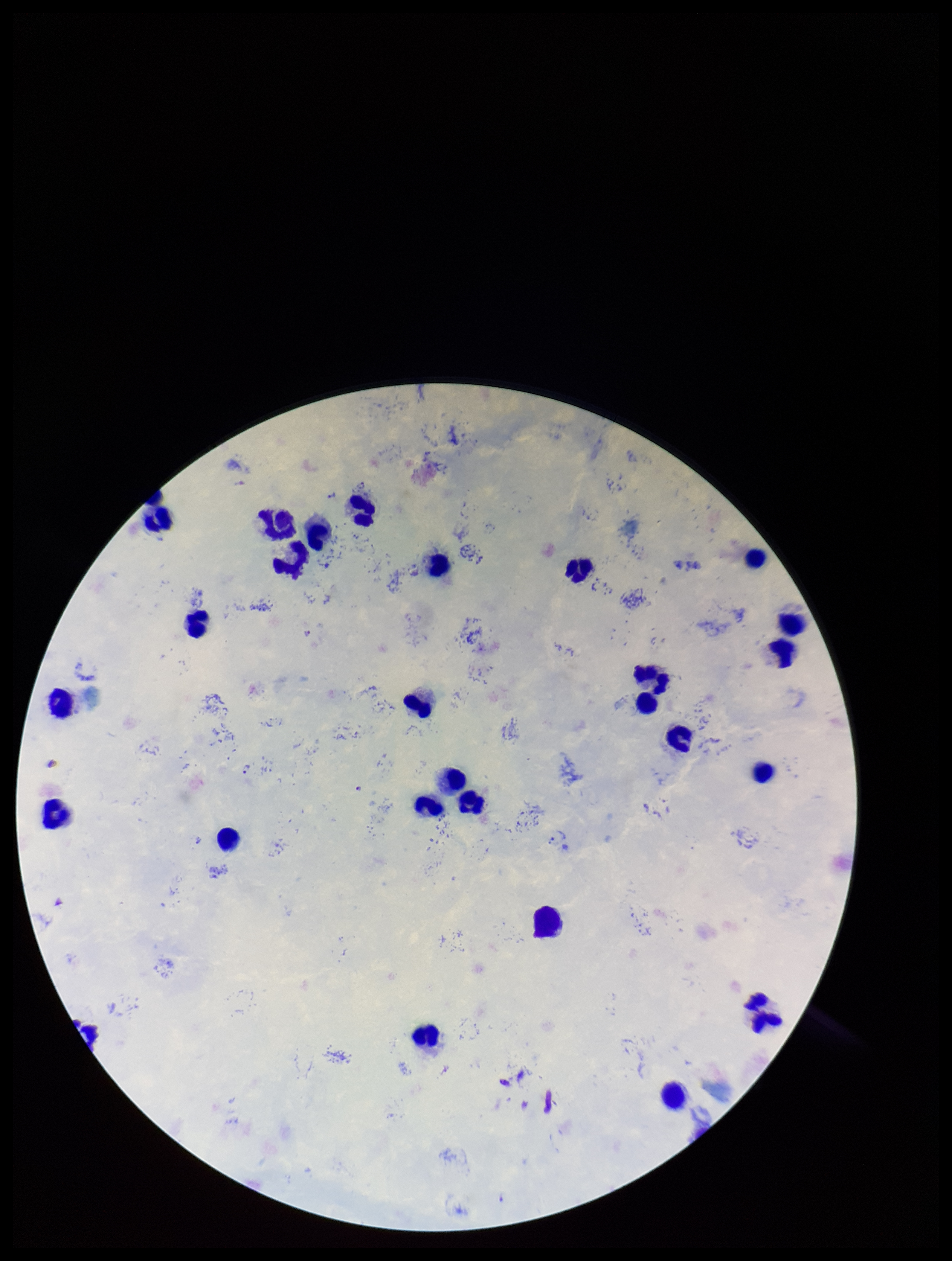
Preparation: thick smear. Plasmodium parasites: seen. Single field of view. Leukocyte count: 25. Smartphone photograph taken through the eyepiece of a microscope. Stained with Giemsa. Patient malaria status: positive. Species reported for this patient: Plasmodium falciparum. Parasite count: 3. Image is 952×1261 pixels.